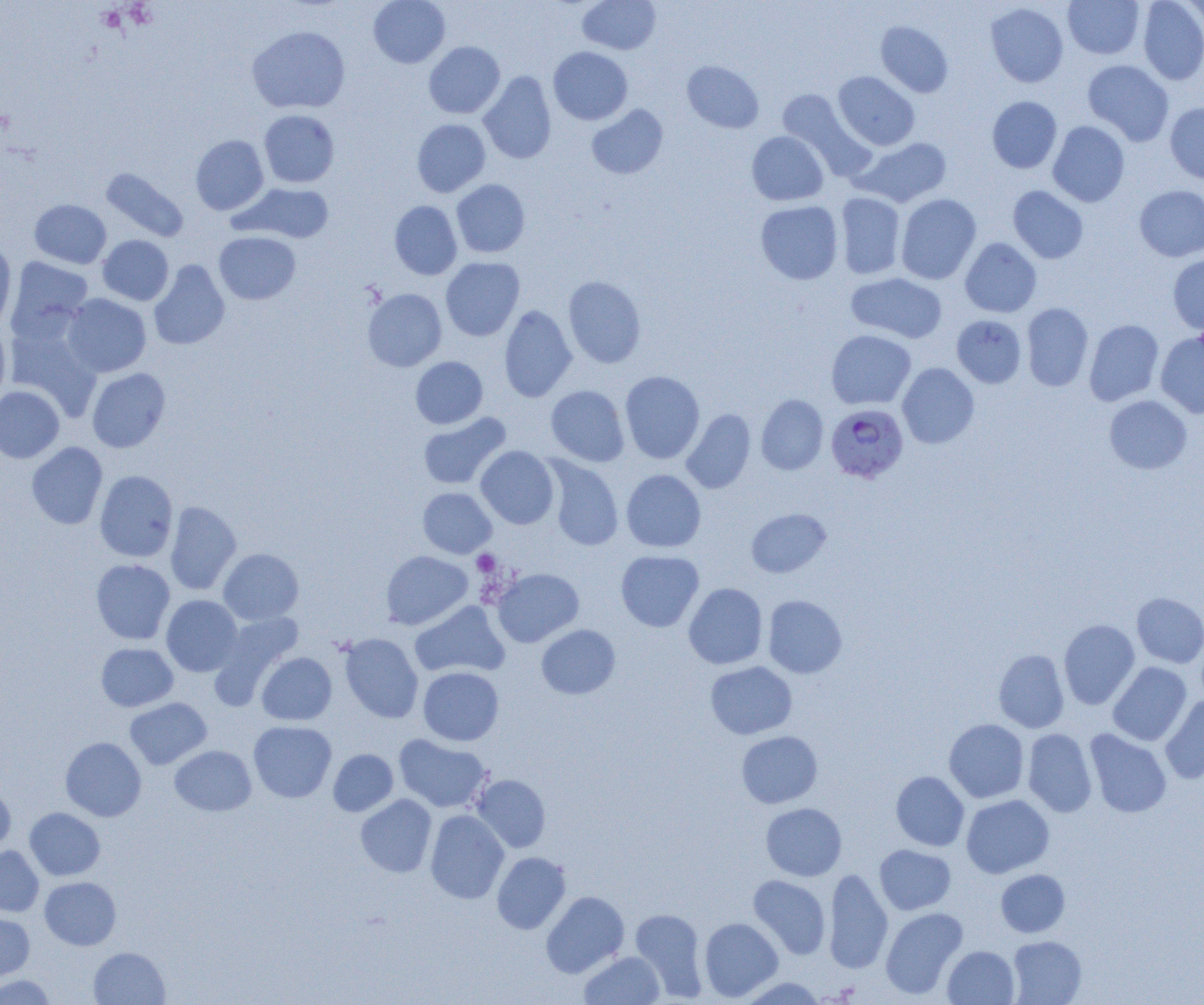 Approximate bounding boxes as named x1/y1/x2/y2 corners in pixels. Uninfected red blood cell locations: (x1=368, y1=0, x2=450, y2=68), (x1=577, y1=0, x2=661, y2=55), (x1=1063, y1=0, x2=1145, y2=59), (x1=1137, y1=0, x2=1204, y2=85), (x1=1181, y1=1, x2=1204, y2=34), (x1=985, y1=3, x2=1069, y2=88), (x1=875, y1=21, x2=954, y2=97), (x1=247, y1=25, x2=351, y2=114), (x1=424, y1=41, x2=505, y2=118), (x1=548, y1=47, x2=633, y2=125), (x1=1082, y1=59, x2=1174, y2=146), (x1=682, y1=60, x2=763, y2=133), (x1=478, y1=71, x2=557, y2=164), (x1=833, y1=71, x2=920, y2=150), (x1=776, y1=89, x2=870, y2=177), (x1=987, y1=96, x2=1062, y2=173), (x1=1165, y1=102, x2=1204, y2=183), (x1=586, y1=104, x2=668, y2=179), (x1=258, y1=109, x2=340, y2=188), (x1=412, y1=119, x2=491, y2=197), (x1=1048, y1=121, x2=1130, y2=207), (x1=747, y1=131, x2=829, y2=206), (x1=190, y1=135, x2=269, y2=215), (x1=857, y1=137, x2=952, y2=207), (x1=101, y1=168, x2=188, y2=242), (x1=451, y1=179, x2=530, y2=257), (x1=230, y1=183, x2=337, y2=243), (x1=1007, y1=185, x2=1088, y2=264), (x1=1134, y1=185, x2=1204, y2=261), (x1=835, y1=192, x2=906, y2=279), (x1=896, y1=194, x2=981, y2=284), (x1=29, y1=199, x2=111, y2=269), (x1=755, y1=200, x2=843, y2=284), (x1=389, y1=201, x2=462, y2=280), (x1=214, y1=232, x2=300, y2=305), (x1=97, y1=235, x2=174, y2=305), (x1=960, y1=238, x2=1041, y2=317), (x1=0, y1=243, x2=17, y2=332), (x1=1167, y1=253, x2=1204, y2=335), (x1=5, y1=256, x2=94, y2=343), (x1=441, y1=257, x2=524, y2=341), (x1=149, y1=260, x2=230, y2=350), (x1=846, y1=272, x2=947, y2=343), (x1=563, y1=275, x2=646, y2=368), (x1=363, y1=288, x2=446, y2=372), (x1=61, y1=293, x2=151, y2=377), (x1=1021, y1=303, x2=1093, y2=391), (x1=498, y1=305, x2=577, y2=402), (x1=951, y1=315, x2=1027, y2=388), (x1=1084, y1=319, x2=1164, y2=406), (x1=0, y1=320, x2=11, y2=405), (x1=4, y1=323, x2=102, y2=420), (x1=826, y1=330, x2=916, y2=409), (x1=1155, y1=332, x2=1204, y2=418), (x1=410, y1=356, x2=488, y2=428), (x1=897, y1=363, x2=979, y2=448), (x1=86, y1=368, x2=171, y2=452), (x1=620, y1=371, x2=705, y2=464), (x1=0, y1=385, x2=64, y2=463), (x1=546, y1=385, x2=630, y2=466), (x1=756, y1=394, x2=829, y2=475), (x1=1104, y1=394, x2=1192, y2=474), (x1=681, y1=408, x2=756, y2=494), (x1=418, y1=412, x2=511, y2=489), (x1=26, y1=442, x2=107, y2=529), (x1=475, y1=446, x2=559, y2=529), (x1=541, y1=457, x2=624, y2=551), (x1=621, y1=469, x2=706, y2=553), (x1=95, y1=470, x2=178, y2=562), (x1=418, y1=487, x2=497, y2=558), (x1=164, y1=500, x2=241, y2=596), (x1=746, y1=508, x2=831, y2=577), (x1=218, y1=548, x2=304, y2=625), (x1=615, y1=549, x2=704, y2=632), (x1=381, y1=551, x2=473, y2=630), (x1=91, y1=559, x2=175, y2=644), (x1=492, y1=568, x2=584, y2=647), (x1=683, y1=582, x2=768, y2=669), (x1=1131, y1=592, x2=1204, y2=668), (x1=161, y1=595, x2=242, y2=676), (x1=763, y1=595, x2=847, y2=678), (x1=410, y1=600, x2=510, y2=679), (x1=213, y1=610, x2=304, y2=698), (x1=1058, y1=619, x2=1140, y2=710), (x1=536, y1=624, x2=620, y2=699), (x1=339, y1=633, x2=423, y2=723), (x1=96, y1=643, x2=178, y2=711), (x1=993, y1=649, x2=1069, y2=733), (x1=257, y1=652, x2=337, y2=725), (x1=705, y1=661, x2=797, y2=739), (x1=1108, y1=662, x2=1191, y2=746), (x1=418, y1=666, x2=504, y2=746), (x1=1160, y1=694, x2=1204, y2=784), (x1=124, y1=697, x2=212, y2=769), (x1=944, y1=718, x2=1029, y2=803), (x1=248, y1=721, x2=337, y2=802), (x1=1023, y1=728, x2=1097, y2=817), (x1=1084, y1=729, x2=1172, y2=818), (x1=736, y1=730, x2=822, y2=808), (x1=393, y1=734, x2=492, y2=813), (x1=60, y1=737, x2=146, y2=821), (x1=170, y1=745, x2=256, y2=816), (x1=328, y1=749, x2=398, y2=816), (x1=891, y1=771, x2=969, y2=851), (x1=471, y1=774, x2=551, y2=853), (x1=0, y1=785, x2=16, y2=854), (x1=356, y1=795, x2=437, y2=877), (x1=961, y1=795, x2=1054, y2=878), (x1=760, y1=802, x2=847, y2=881), (x1=24, y1=807, x2=105, y2=880), (x1=426, y1=810, x2=509, y2=904), (x1=875, y1=844, x2=956, y2=915), (x1=0, y1=846, x2=44, y2=917), (x1=492, y1=851, x2=571, y2=935), (x1=824, y1=868, x2=893, y2=973), (x1=996, y1=869, x2=1070, y2=937), (x1=748, y1=875, x2=831, y2=960), (x1=40, y1=876, x2=121, y2=950), (x1=541, y1=890, x2=629, y2=978), (x1=880, y1=907, x2=968, y2=999), (x1=631, y1=908, x2=708, y2=1000), (x1=0, y1=912, x2=35, y2=981), (x1=699, y1=917, x2=783, y2=1001), (x1=1008, y1=936, x2=1086, y2=1004), (x1=942, y1=945, x2=1019, y2=1004), (x1=89, y1=947, x2=170, y2=1004), (x1=578, y1=950, x2=665, y2=1005), (x1=0, y1=974, x2=57, y2=1004), (x1=736, y1=977, x2=828, y2=1004). Platelet locations: (x1=472, y1=550, x2=500, y2=576). Plasmodium falciparum-infected red blood cell locations: (x1=826, y1=404, x2=908, y2=483). Slide-level diagnosis: Plasmodium falciparum. Image is 1204×1005 pixels. Optical microscopy. Thin blood smear. Single field of view. 1000x magnification.